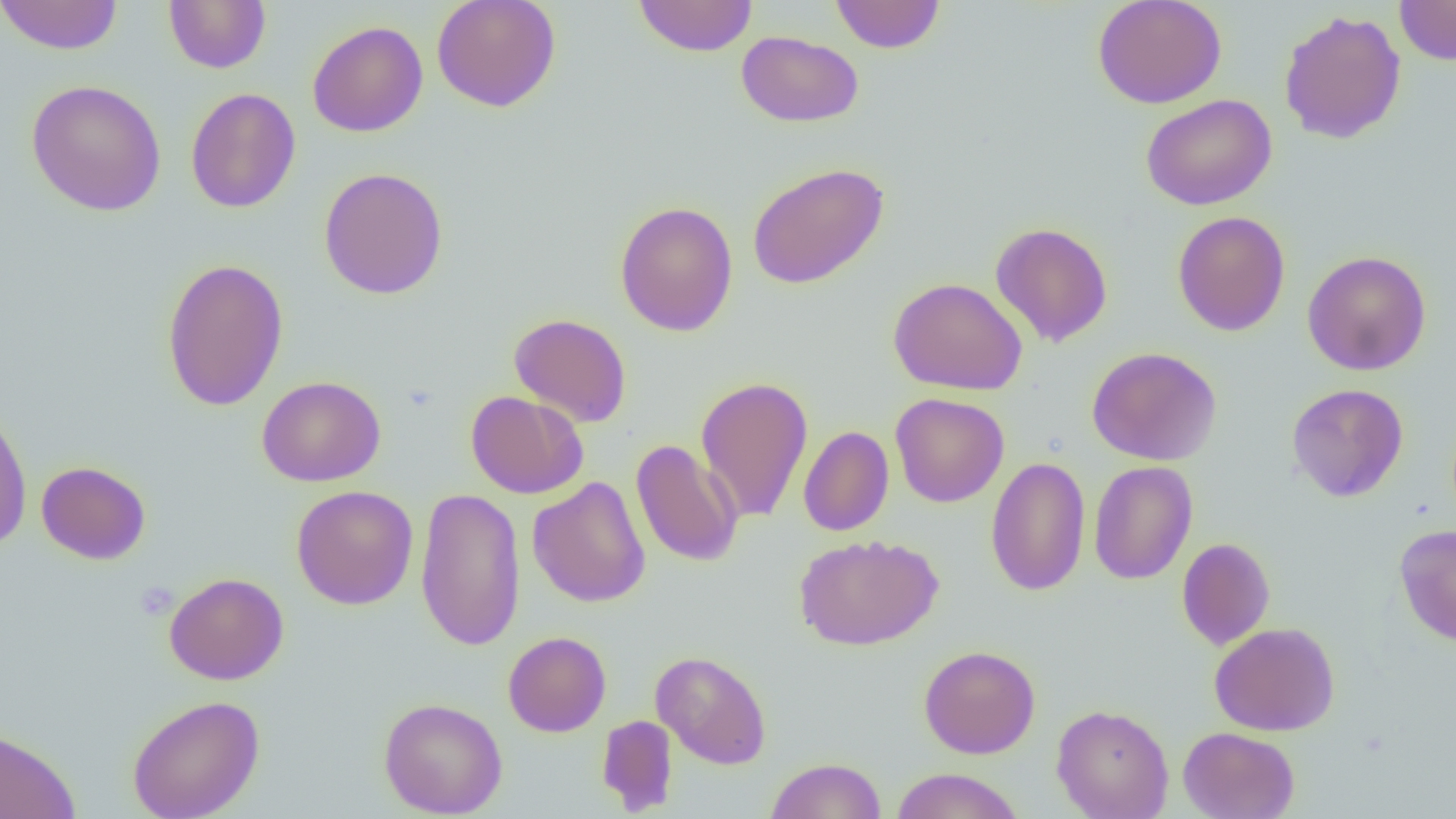
slide-level diagnosis = no evidence of blood parasites
field of view = single
image size = 1456×819 pixels
preparation = thin blood smear
uninfected red blood cell locations = approximate bounding boxes as (x1, y1, x2, y2) in pixels: (0, 0, 124, 55), (431, 0, 561, 112), (633, 0, 758, 57), (830, 0, 945, 53), (1092, 0, 1227, 109), (1395, 0, 1456, 65), (163, 1, 271, 73), (1278, 9, 1407, 145), (307, 20, 428, 138), (736, 30, 864, 128), (26, 79, 166, 216), (186, 87, 301, 213), (1141, 94, 1276, 211), (747, 162, 889, 289), (318, 167, 449, 299), (614, 200, 738, 336), (1172, 210, 1290, 336), (990, 222, 1113, 347), (1302, 250, 1431, 376), (160, 257, 289, 411), (888, 277, 1028, 396), (509, 313, 632, 427), (1087, 346, 1221, 466), (257, 375, 386, 487), (695, 375, 813, 524), (1286, 383, 1409, 502), (465, 390, 588, 499), (889, 393, 1009, 508), (0, 402, 32, 552), (799, 426, 894, 536), (630, 439, 743, 568), (985, 456, 1091, 596), (36, 460, 151, 565), (1088, 461, 1198, 585), (528, 477, 651, 607), (291, 485, 419, 610), (415, 486, 526, 652), (1394, 523, 1456, 645), (794, 534, 942, 651), (1176, 537, 1275, 650), (164, 572, 289, 685), (1209, 621, 1340, 736), (503, 631, 611, 737), (918, 644, 1040, 759), (651, 650, 772, 769), (127, 694, 265, 819), (378, 697, 508, 818), (1051, 703, 1174, 818), (596, 714, 678, 815), (0, 726, 81, 819), (1178, 727, 1300, 819), (765, 757, 887, 818), (890, 767, 1025, 819)
magnification = 1000x
modality = optical microscopy
platelet locations = approximate bounding boxes as (x1, y1, x2, y2) in pixels: (136, 580, 178, 622)